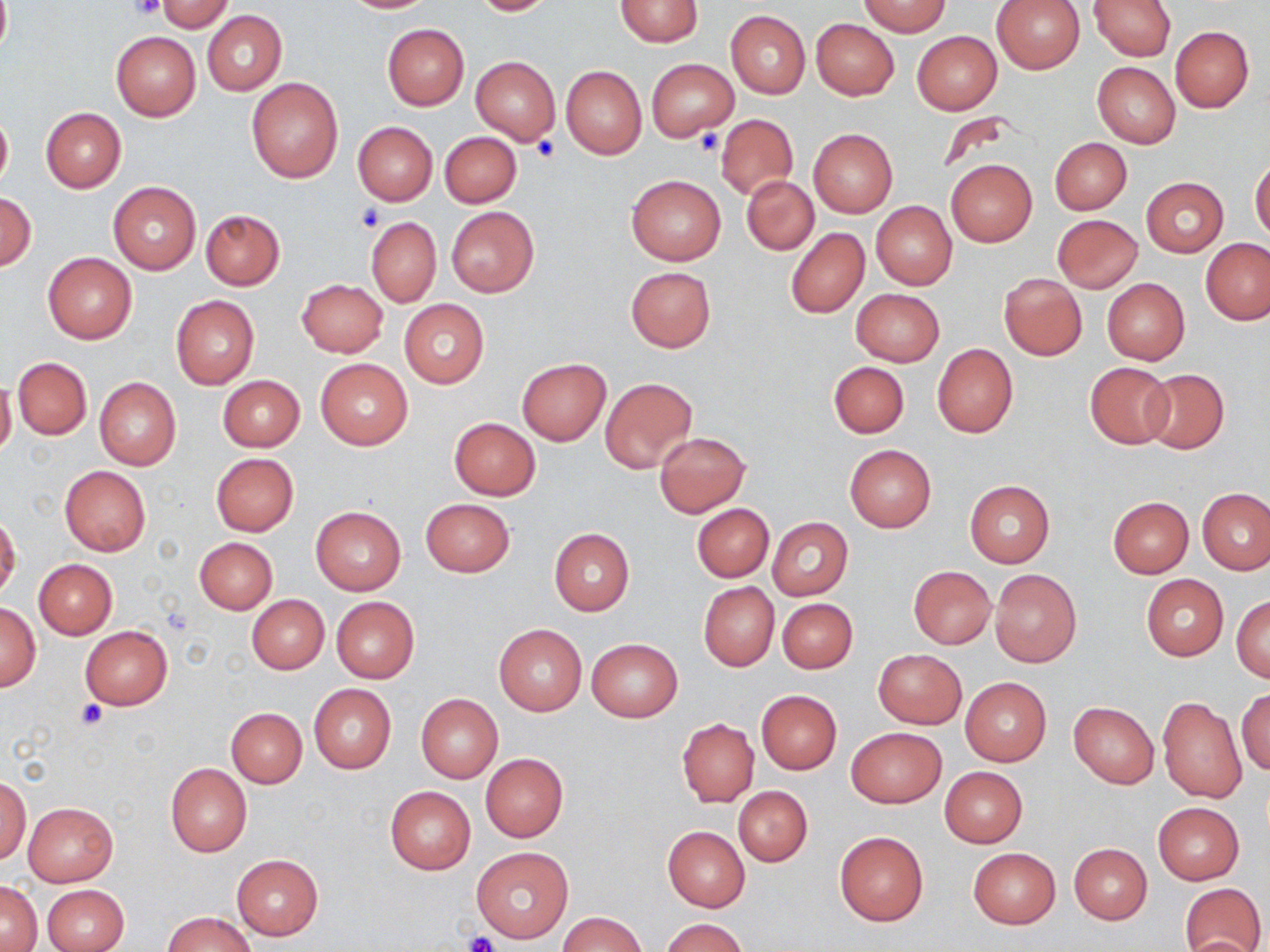 Approximate bounding boxes as (x1, y1, x2, y2) in pixels. Uninfected red blood cell locations: (338, 0, 437, 13), (469, 0, 558, 15), (614, 0, 703, 47), (859, 0, 951, 36), (991, 0, 1085, 73), (0, 1, 12, 57), (155, 1, 234, 33), (1089, 1, 1177, 60), (726, 10, 809, 98), (201, 11, 285, 96), (811, 18, 899, 100), (382, 23, 469, 110), (1170, 25, 1253, 112), (912, 31, 1002, 115), (111, 32, 200, 120), (470, 55, 560, 145), (647, 59, 738, 141), (1091, 62, 1180, 148), (561, 66, 646, 159), (246, 77, 344, 184), (0, 107, 13, 192), (40, 107, 126, 192), (939, 112, 1013, 176), (716, 115, 798, 198), (353, 121, 437, 204), (809, 128, 898, 217), (439, 131, 521, 208), (1050, 137, 1132, 215), (1250, 158, 1270, 241), (946, 159, 1037, 247), (626, 175, 727, 265), (743, 177, 819, 255), (1141, 177, 1228, 257), (108, 180, 202, 274), (1, 193, 36, 269), (870, 200, 957, 289), (446, 207, 539, 297), (199, 209, 285, 290), (1052, 214, 1142, 292), (366, 215, 441, 308), (786, 228, 869, 318), (1201, 238, 1269, 325), (43, 253, 137, 344), (625, 267, 715, 352), (999, 273, 1087, 359), (1102, 277, 1189, 365), (296, 279, 388, 358), (851, 288, 945, 366), (170, 295, 260, 389), (399, 300, 489, 389), (932, 343, 1018, 439), (12, 357, 91, 440), (315, 358, 412, 450), (517, 359, 610, 445), (829, 361, 909, 438), (1084, 362, 1175, 449), (1139, 368, 1230, 454), (218, 375, 304, 451), (94, 377, 182, 470), (600, 377, 698, 472), (0, 378, 17, 461), (449, 417, 540, 500), (654, 433, 751, 517), (845, 444, 936, 532), (211, 453, 298, 536), (59, 466, 151, 555), (965, 481, 1056, 569), (1197, 488, 1269, 574), (1107, 496, 1192, 577), (420, 498, 515, 577), (692, 504, 773, 581), (310, 505, 407, 595), (0, 512, 20, 600), (767, 518, 853, 601), (549, 528, 634, 614), (194, 537, 278, 614), (34, 559, 117, 638), (908, 565, 996, 649), (990, 569, 1081, 668), (1140, 574, 1229, 660), (698, 582, 779, 670), (247, 594, 328, 673), (1232, 595, 1269, 683), (331, 597, 420, 682), (777, 598, 857, 673), (0, 602, 40, 689), (494, 623, 586, 716), (80, 625, 172, 707), (588, 638, 682, 722), (873, 649, 967, 729), (960, 677, 1051, 766), (309, 684, 395, 773), (1236, 688, 1270, 776), (756, 690, 841, 774), (416, 694, 503, 783), (1158, 696, 1247, 803), (1068, 701, 1158, 788), (226, 707, 307, 788), (677, 718, 759, 806), (846, 726, 946, 807), (481, 753, 568, 841), (166, 763, 251, 856), (940, 767, 1027, 847), (1, 776, 31, 864), (385, 786, 476, 874), (734, 786, 812, 866), (21, 801, 118, 888), (1153, 803, 1244, 884), (663, 826, 750, 911), (833, 829, 930, 926), (1068, 843, 1152, 925), (472, 845, 574, 943), (968, 847, 1060, 928), (231, 853, 324, 941), (1, 880, 40, 951), (1180, 882, 1267, 952), (43, 884, 128, 952), (163, 911, 256, 952), (559, 912, 646, 952), (660, 917, 749, 952), (1179, 934, 1263, 951). Platelet locations: (128, 0, 163, 20), (696, 126, 725, 156), (532, 134, 559, 160), (357, 203, 384, 233), (75, 699, 108, 730), (464, 932, 501, 952). Slide-level diagnosis: negative for blood parasites. Image is 1270×952 pixels. Captured at 1000x magnification. One field of a larger specimen. Thin blood smear. Optical microscopy. May-Grünwald-Giemsa stain.